Name the blood parasite species.
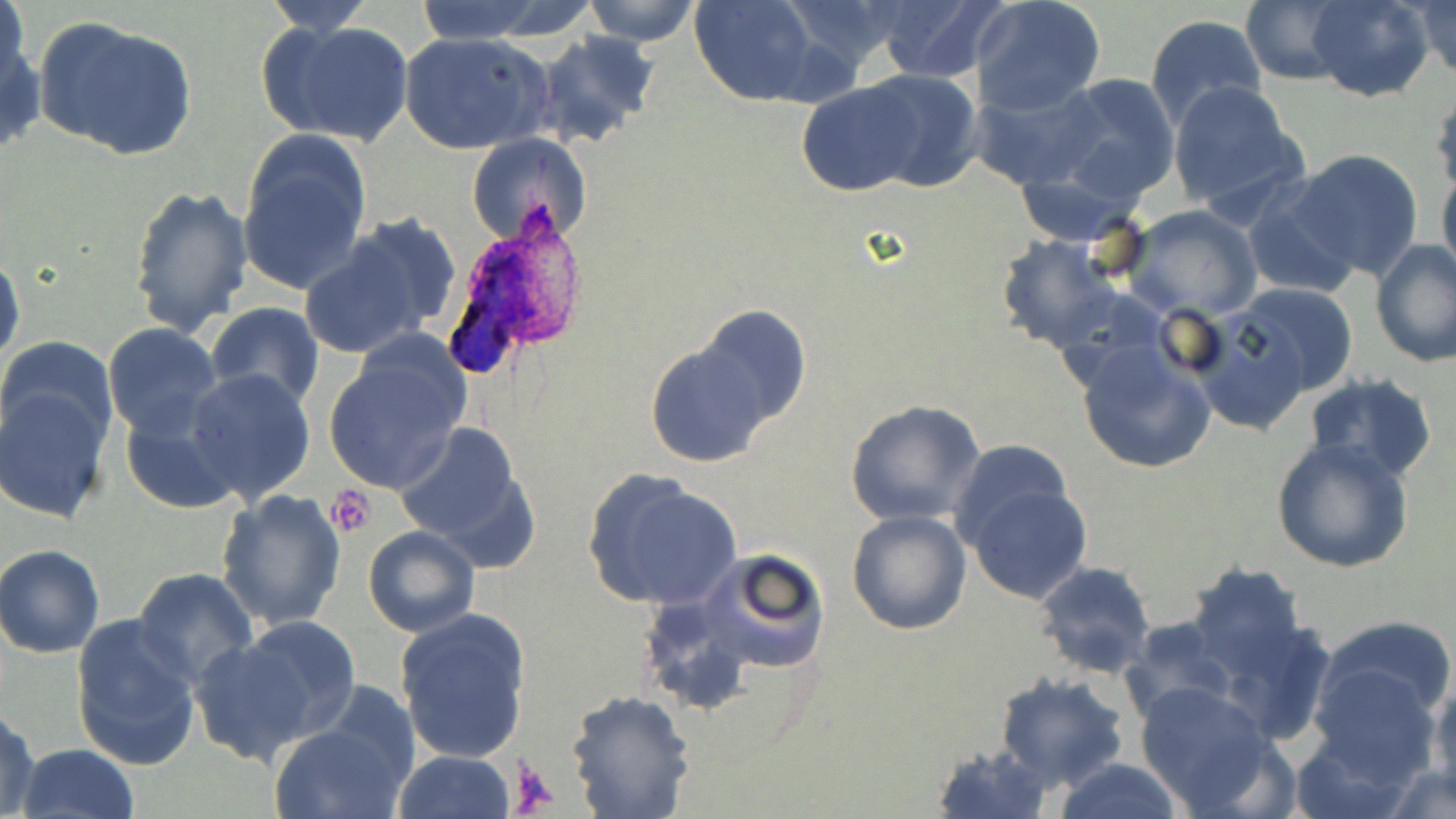

Plasmodium ovale.

Summary:
  - Coordinate format: approximate bounding boxes as [x1, y1, x2, y2] in pixels
  - Platelet locations: [330, 486, 377, 535], [508, 757, 560, 812]
  - Plasmodium ovale-infected red blood cell locations: [438, 228, 570, 382]
  - Uninfected red blood cell locations: [2, 0, 32, 96], [408, 0, 564, 44], [577, 0, 703, 47], [689, 0, 819, 107], [971, 0, 1107, 117], [1240, 0, 1351, 85], [1304, 0, 1434, 102], [871, 1, 1005, 83], [1412, 1, 1455, 83], [259, 2, 379, 34], [1144, 13, 1267, 129], [34, 16, 197, 161], [262, 17, 414, 148], [0, 24, 45, 157], [530, 31, 660, 148], [398, 32, 554, 156], [852, 68, 984, 194], [1047, 72, 1181, 206], [795, 81, 924, 196], [968, 81, 1110, 192], [1167, 81, 1307, 217], [1431, 89, 1456, 201], [237, 134, 372, 295], [466, 135, 587, 245], [1285, 149, 1427, 283], [1439, 169, 1456, 287], [129, 183, 254, 336], [1239, 186, 1360, 300], [1122, 205, 1264, 323], [299, 218, 456, 360], [995, 232, 1123, 352], [1370, 239, 1454, 370], [0, 250, 26, 372], [1229, 283, 1359, 398], [203, 304, 325, 412], [1191, 305, 1325, 436], [102, 323, 224, 440], [643, 325, 793, 469], [324, 336, 472, 493], [1, 337, 118, 450], [1075, 341, 1218, 474], [184, 368, 316, 506], [1304, 374, 1438, 486], [0, 380, 115, 525], [844, 398, 985, 526], [119, 402, 242, 514], [392, 420, 540, 561], [1272, 438, 1414, 574], [951, 439, 1075, 554], [583, 471, 744, 611], [959, 477, 1092, 603], [214, 489, 348, 633], [846, 510, 972, 635], [363, 525, 481, 638], [0, 545, 105, 657], [692, 546, 833, 678], [1033, 560, 1159, 682], [1187, 560, 1310, 681], [131, 567, 258, 686], [395, 607, 531, 765], [70, 613, 201, 774], [234, 615, 362, 742], [1317, 615, 1456, 730], [1119, 618, 1236, 725], [190, 632, 325, 767], [1304, 661, 1442, 785], [993, 672, 1131, 792], [1427, 679, 1456, 804], [1131, 680, 1283, 815], [565, 688, 695, 819], [0, 709, 41, 819], [269, 712, 412, 819], [930, 740, 1052, 818], [16, 743, 142, 819], [393, 750, 517, 819], [1053, 759, 1185, 818], [1380, 763, 1456, 818]
  - Image size: 1456×819 pixels
  - Preparation: thin blood film
  - Field of view: one of a larger specimen
  - Stain: May-Grünwald-Giemsa
  - Modality: light microscopy
  - Magnification: 1000x